State which parasite is depicted.
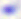

Toxoplasma gondii.

Micrograph. 400x magnification.